Outline platelets.
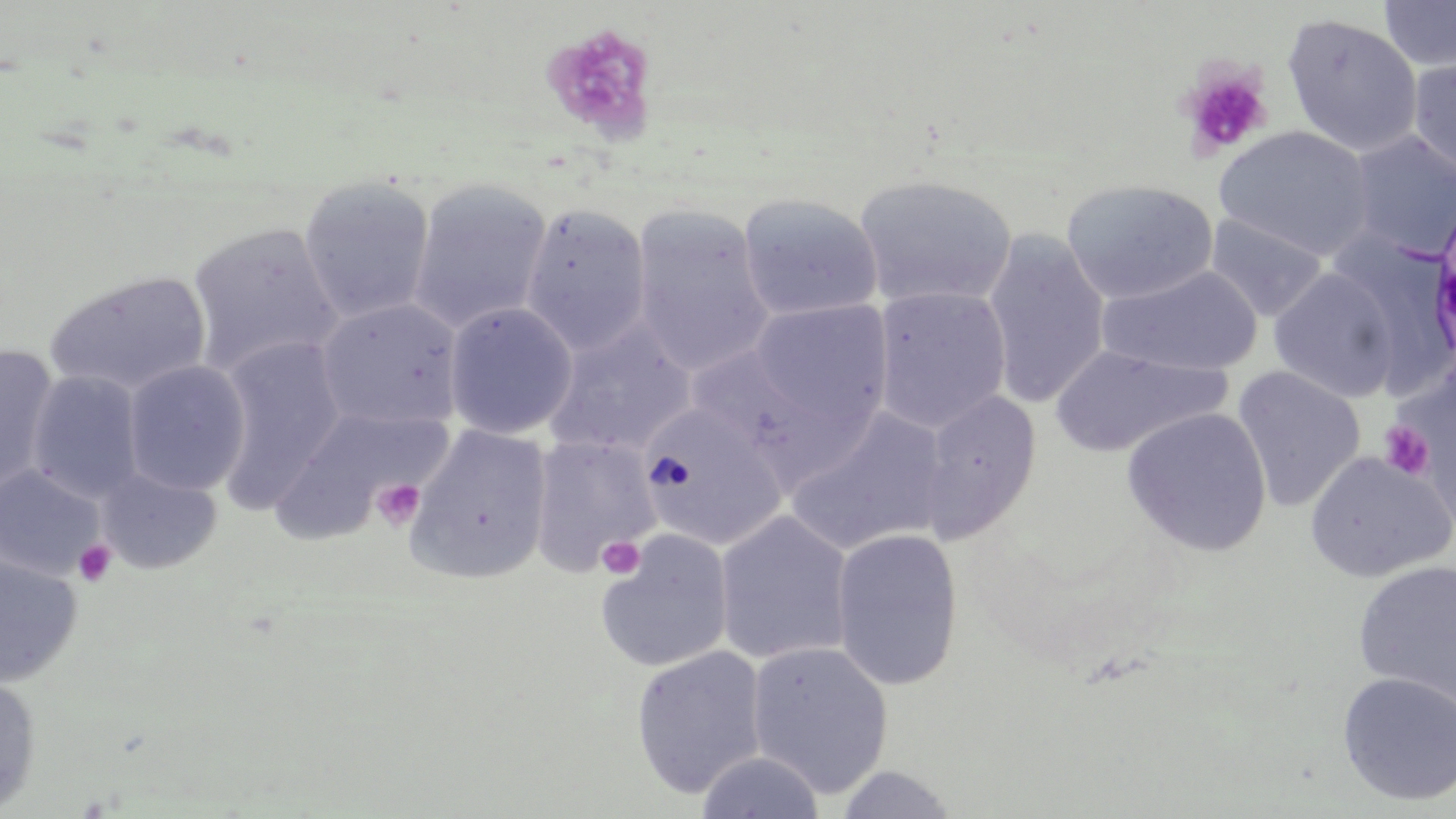

Approximate bounding boxes as (x1, y1, x2, y2) in pixels.
Platelets: (540, 23, 659, 145), (1178, 62, 1273, 161), (1379, 420, 1435, 480), (372, 478, 426, 532), (597, 535, 646, 580), (73, 539, 117, 587).

slide_level_diagnosis: no evidence of blood parasites
stain: May-Grünwald-Giemsa
image_size: 1456×819 pixels
modality: light microscopy
preparation: thin blood smear
field_of_view: one of a larger specimen
uninfected_red_blood_cell_locations: 'approximate bounding boxes as (x1, y1, x2, y2) in pixels: (1379, 0, 1456, 73), (1281, 13, 1424, 158), (1407, 57, 1456, 180), (1213, 125, 1376, 261), (1344, 130, 1456, 260), (852, 172, 1017, 309), (297, 175, 436, 324), (1060, 178, 1219, 305), (407, 179, 553, 335), (737, 192, 883, 323), (519, 203, 652, 355), (629, 204, 775, 378), (1204, 211, 1329, 323), (186, 221, 343, 379), (981, 230, 1110, 411), (1325, 232, 1456, 392), (1098, 265, 1263, 376), (1268, 267, 1402, 402), (45, 269, 212, 397), (872, 286, 1012, 434), (315, 297, 464, 432), (749, 300, 893, 434), (444, 301, 578, 439), (545, 321, 696, 458), (212, 334, 346, 509), (0, 343, 60, 496), (1049, 345, 1229, 457), (122, 360, 251, 496), (1231, 366, 1366, 513), (26, 370, 145, 504), (917, 389, 1041, 544), (639, 401, 788, 551), (271, 405, 447, 541), (784, 407, 951, 557), (1121, 407, 1272, 557), (406, 425, 553, 584), (529, 435, 660, 577), (1304, 450, 1454, 582), (1, 465, 106, 581), (94, 465, 223, 575), (714, 511, 855, 666), (830, 528, 963, 692), (594, 530, 734, 674), (0, 553, 82, 688), (1352, 558, 1456, 711), (746, 640, 894, 799), (630, 645, 768, 798), (1336, 671, 1456, 806), (0, 673, 42, 816), (694, 750, 825, 819), (834, 765, 960, 819)'
magnification: 1000x